State the preparation type.
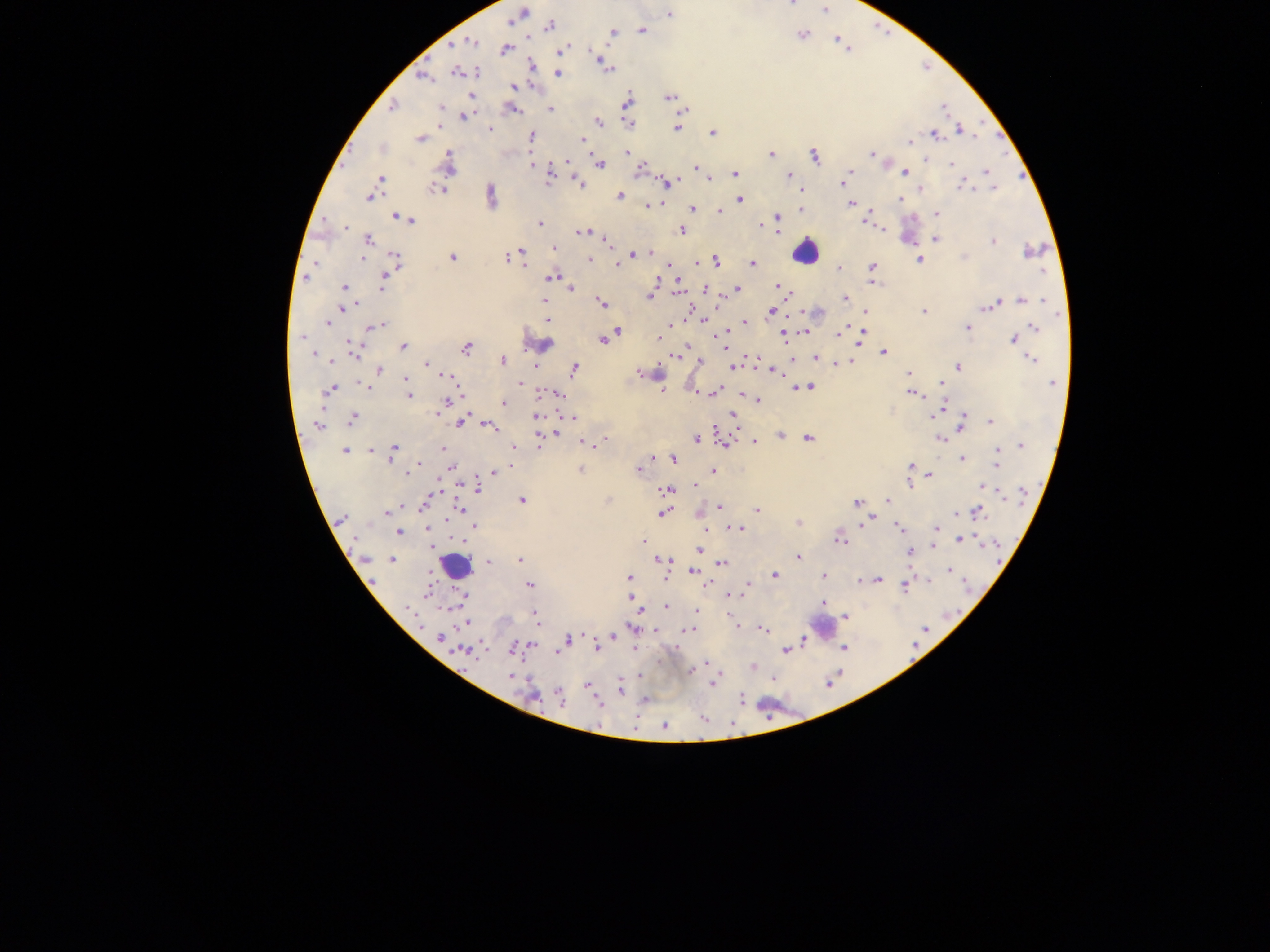
This is a thick smear.

malaria parasite locations = approximate centers as {x, y} in pixels: {791, 5}, {824, 10}, {522, 13}, {670, 13}, {550, 25}, {642, 30}, {613, 32}, {802, 34}, {472, 41}, {839, 41}, {505, 49}, {563, 50}, {598, 58}, {603, 62}, {606, 67}, {457, 72}, {476, 72}, {558, 72}, {422, 76}, {514, 86}, {670, 97}, {627, 102}, {392, 106}, {440, 108}, {513, 109}, {550, 109}, {466, 116}, {598, 122}, {628, 123}, {678, 127}, {490, 129}, {960, 130}, {713, 132}, {934, 134}, {532, 136}, {420, 138}, {582, 140}, {910, 142}, {628, 152}, {771, 154}, {871, 154}, {815, 156}, {566, 161}, {448, 164}, {533, 164}, {570, 164}, {601, 164}, {951, 165}, {695, 168}, {640, 170}, {903, 172}, {986, 172}, {735, 174}, {550, 175}, {789, 175}, {847, 177}, {379, 179}, {709, 179}, {844, 182}, {579, 183}, {668, 183}, {963, 186}, {993, 187}, {919, 188}, {437, 189}, {491, 195}, {619, 195}, {369, 196}, {739, 199}, {899, 199}, {851, 204}, {647, 205}, {693, 208}, {801, 208}, {719, 211}, {936, 214}, {397, 217}, {409, 219}, {777, 219}, {868, 222}, {541, 223}, {761, 226}, {346, 227}, {681, 230}, {585, 232}, {936, 239}, {367, 240}, {606, 242}, {993, 242}, {554, 248}, {1031, 250}, {522, 251}, {649, 253}, {632, 254}, {452, 257}, {506, 258}, {362, 259}, {396, 259}, {589, 260}, {920, 260}, {716, 261}, {315, 263}, {617, 263}, {697, 263}, {753, 263}, {871, 267}, {839, 269}, {306, 276}, {552, 277}, {657, 280}, {678, 281}, {383, 284}, {344, 287}, {777, 287}, {571, 289}, {705, 289}, {737, 289}, {650, 296}, {844, 299}, {545, 300}, {1022, 301}, {602, 302}, {991, 304}, {343, 309}, {922, 311}, {771, 312}, {865, 313}, {702, 318}, {547, 319}, {745, 322}, {328, 323}, {381, 325}, {371, 326}, {968, 327}, {1035, 327}, {618, 331}, {805, 332}, {613, 333}, {783, 333}, {837, 334}, {724, 335}, {301, 337}, {659, 338}, {860, 338}, {1012, 339}, {603, 340}, {546, 344}, {403, 347}, {466, 348}, {354, 351}, {884, 352}, {313, 354}, {676, 356}, {792, 359}, {816, 359}, {1031, 359}, {502, 360}, {699, 362}, {426, 364}, {838, 364}, {536, 366}, {957, 366}, {734, 367}, {379, 369}, {574, 369}, {776, 372}, {640, 373}, {647, 373}, {908, 374}, {447, 376}, {406, 379}, {520, 383}, {942, 383}, {1052, 383}, {364, 385}, {808, 387}, {798, 388}, {332, 389}, {716, 390}, {912, 393}, {556, 394}, {408, 395}, {447, 400}, {758, 400}, {503, 402}, {941, 409}, {438, 412}, {933, 414}, {536, 416}, {733, 416}, {572, 417}, {352, 420}, {460, 421}, {992, 422}, {962, 423}, {318, 425}, {488, 427}, {555, 433}, {780, 436}, {808, 438}, {940, 438}, {696, 439}, {605, 440}, {724, 442}, {754, 442}, {584, 443}, {539, 445}, {591, 445}, {1021, 445}, {514, 446}, {443, 448}, {393, 449}, {371, 450}, {344, 451}, {390, 456}, {963, 458}, {674, 459}, {997, 461}, {417, 465}, {511, 466}, {910, 467}, {414, 468}, {451, 468}, {580, 469}, {638, 470}, {714, 471}, {408, 472}, {496, 472}, {930, 475}, {910, 481}, {696, 485}, {984, 488}, {479, 489}, {667, 490}, {523, 500}, {887, 500}, {857, 502}, {424, 505}, {719, 507}, {757, 509}, {459, 510}, {387, 512}, {976, 512}, {663, 513}, {341, 519}, {798, 523}, {865, 523}, {474, 526}, {899, 527}, {428, 528}, {738, 529}, {937, 529}, {399, 532}, {839, 539}, {962, 539}, {643, 540}, {698, 550}, {909, 553}, {798, 556}, {521, 559}, {392, 560}, {664, 560}, {488, 561}, {722, 563}, {949, 570}, {694, 571}, {774, 575}, {823, 576}, {629, 578}, {876, 579}, {860, 581}, {905, 584}, {530, 585}, {427, 593}, {463, 596}, {731, 596}, {630, 598}, {823, 603}, {666, 606}, {408, 607}, {697, 611}, {534, 614}, {847, 617}, {465, 623}, {689, 629}, {763, 629}, {440, 637}, {566, 638}, {597, 646}, {515, 647}, {843, 648}, {559, 650}, {785, 651}, {465, 652}, {706, 663}, {753, 666}, {690, 671}, {510, 676}, {714, 683}, {588, 686}, {620, 688}, {534, 695}, {560, 698}, {741, 699}, {645, 700}, {598, 702}, {665, 726}
image size = 1270×952 pixels
capture = mobile-phone photograph through a microscope
field of view = single
leukocyte locations = approximate centers as {x, y} in pixels: {803, 252}, {455, 565}, {822, 625}
country = Ghana